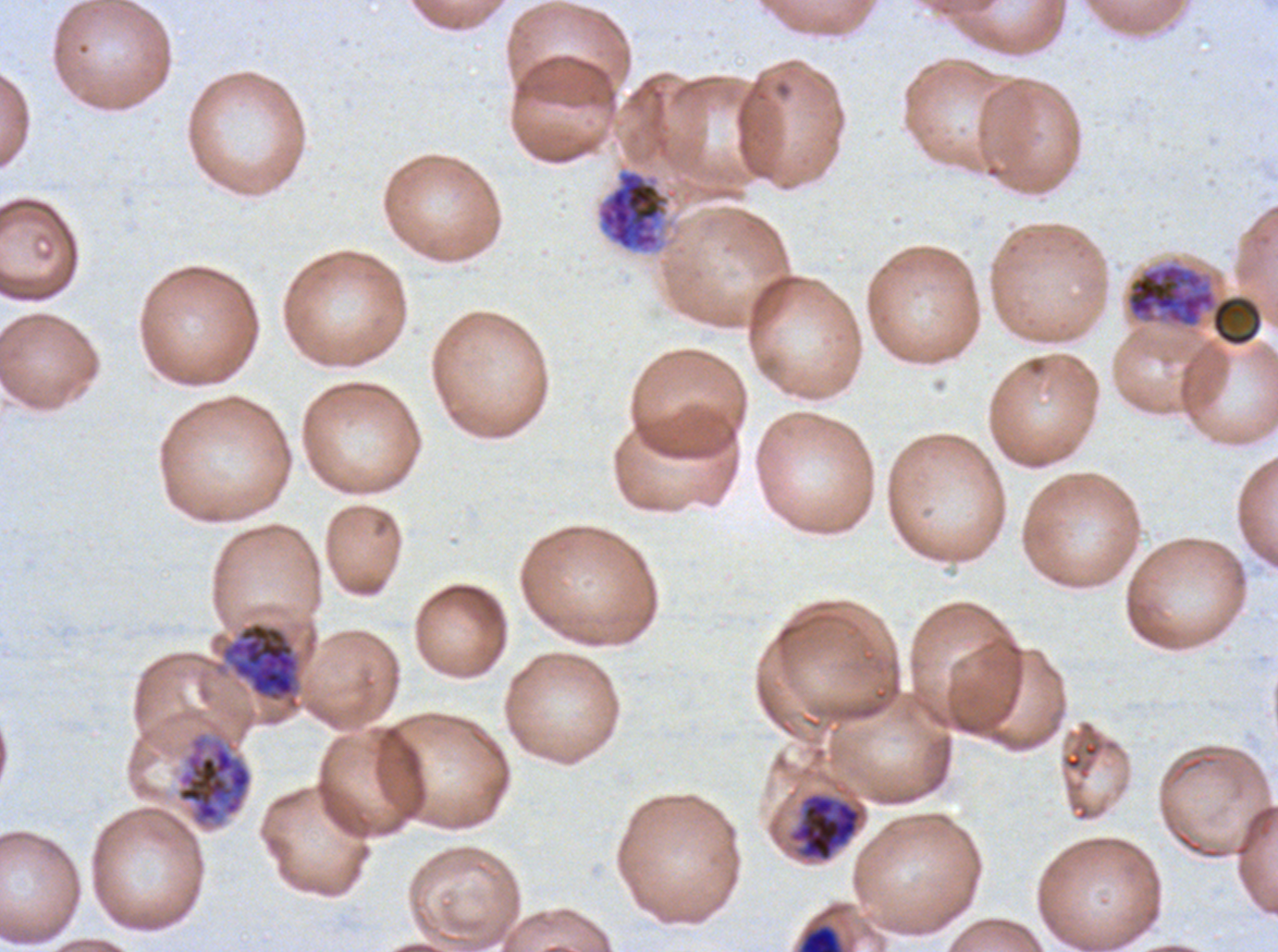

Approximate bounding boxes as (x1, y1, x2, y2) in pixels. Late schizont locations: (799, 925, 842, 951). Early schizont locations: (596, 168, 678, 255), (1126, 262, 1264, 348), (222, 621, 300, 708), (175, 729, 253, 831), (790, 792, 862, 862). Debris locations: (1126, 262, 1264, 348) (two touching objects share this one region). Giemsa-stained preparation. Image is 1278×952 pixels. Life-cycle stages observed: early schizont, late schizont. Plasmodium falciparum from a patient in The Gambia, cultured ex vivo for 24 to 48 hours. A sub-image separated from a larger composite. Thin blood smear.